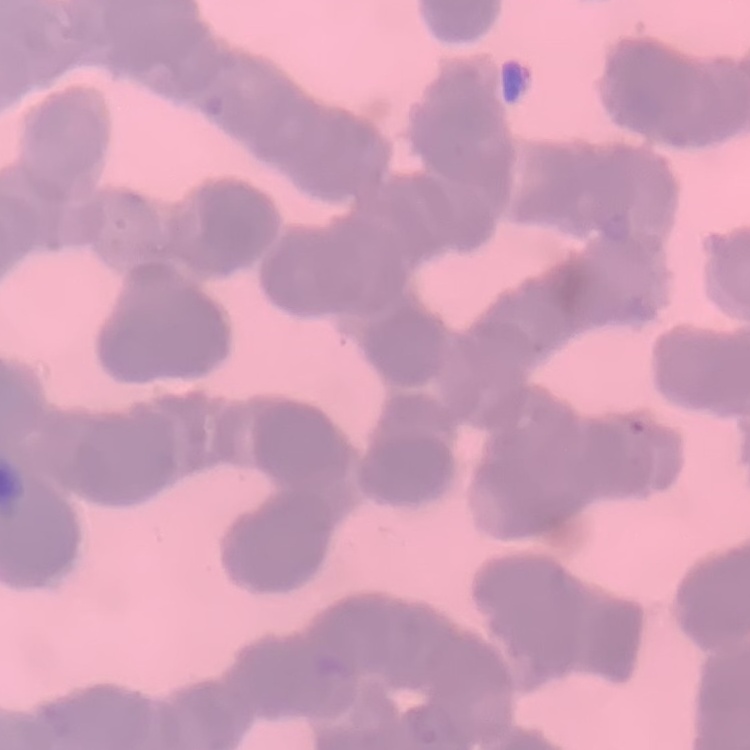

red blood cell morphology = rouleaux formation
preparation = thin blood smear
image type = one tile cut from a larger photomicrograph
stain = Field's or Giemsa